Mark where platelets are.
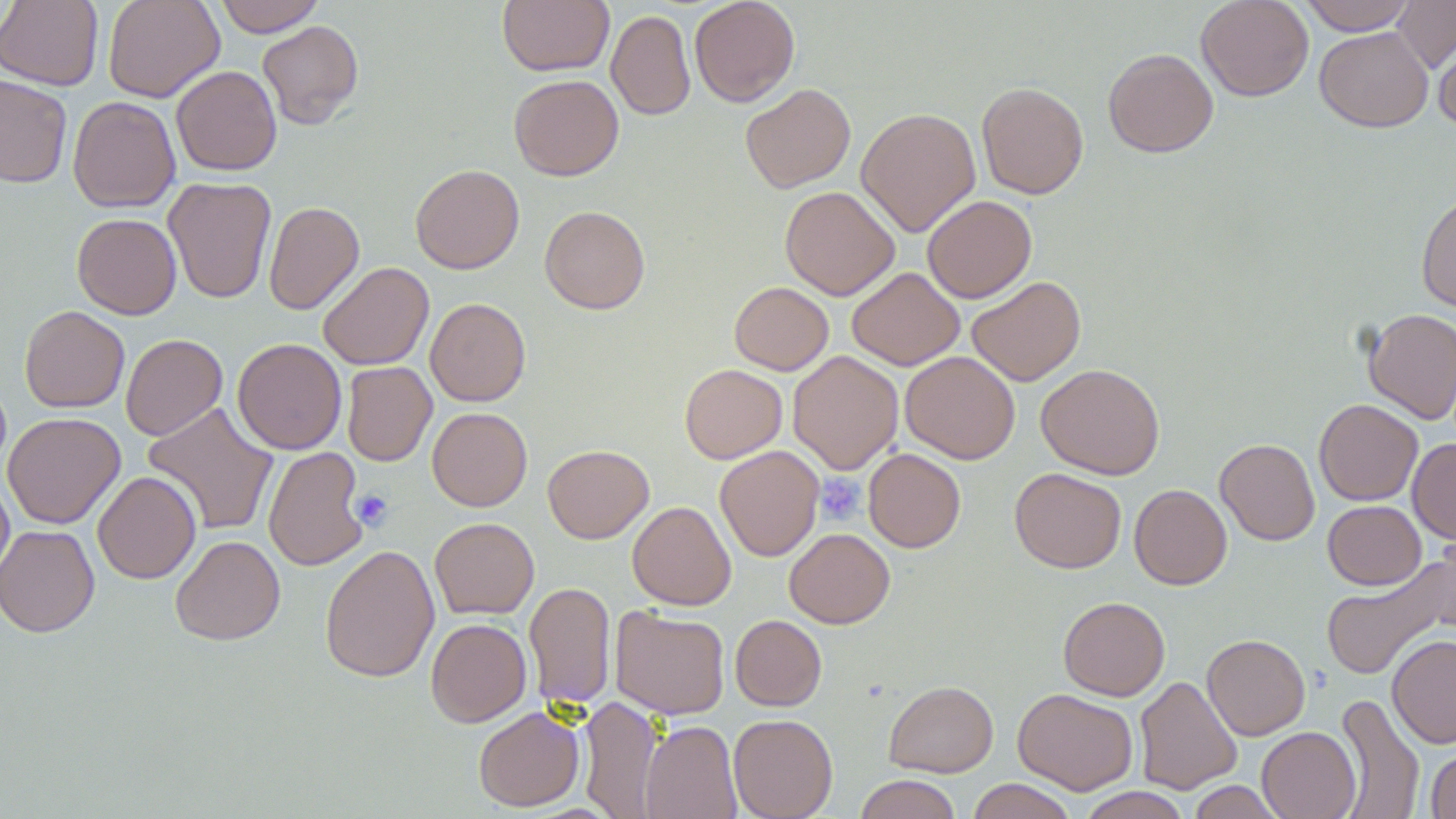

Approximate bounding boxes as (x1,y1)-(x2,y2) corner pairs in pixels.
Platelets: (815,474)-(864,526), (350,488)-(394,531).

Uninfected red blood cell locations: (102,0)-(224,102), (214,0)-(326,36), (497,0)-(614,76), (689,0)-(800,107), (1195,0)-(1314,102), (1299,0)-(1417,35), (1391,0)-(1456,73), (0,1)-(103,90), (606,10)-(695,120), (257,20)-(364,129), (1315,26)-(1433,132), (1432,28)-(1456,133), (1103,48)-(1218,158), (171,66)-(282,175), (509,74)-(624,181), (0,75)-(72,187), (976,82)-(1088,199), (740,83)-(856,193), (68,96)-(181,213), (856,107)-(981,237), (410,164)-(524,274), (163,177)-(277,304), (779,186)-(900,300), (1415,190)-(1456,313), (922,195)-(1037,303), (263,201)-(364,315), (540,206)-(650,314), (71,213)-(182,319), (318,262)-(434,370), (847,267)-(964,370), (966,276)-(1086,386), (729,281)-(833,375), (425,298)-(531,406), (19,305)-(129,413), (1362,308)-(1456,424), (120,333)-(228,440), (232,338)-(346,455), (788,350)-(904,474), (900,351)-(1020,464), (341,361)-(437,467), (1036,363)-(1165,480), (679,364)-(787,464), (1313,399)-(1423,506), (142,402)-(279,536), (427,407)-(532,511), (3,412)-(125,529), (1408,437)-(1456,544), (1215,439)-(1320,545), (542,444)-(654,543), (263,446)-(369,571), (715,446)-(824,561), (863,448)-(966,553), (1009,468)-(1126,573), (92,471)-(201,584), (0,474)-(14,585), (1129,484)-(1232,590), (1323,500)-(1426,590), (627,501)-(736,610), (429,517)-(539,619), (0,525)-(100,637), (784,528)-(895,628), (170,535)-(285,645), (320,544)-(439,683), (1320,561)-(1454,681), (524,581)-(616,711), (1058,596)-(1170,701), (609,606)-(730,719), (730,615)-(827,711), (425,618)-(531,727), (1202,634)-(1310,740), (1387,634)-(1456,748), (1134,675)-(1243,795), (883,680)-(999,777), (1013,688)-(1138,795), (1333,694)-(1425,819), (578,695)-(662,819), (473,706)-(584,811), (728,713)-(838,819), (640,720)-(742,819), (1257,726)-(1361,818), (1425,747)-(1456,818), (854,774)-(962,819), (966,778)-(1077,819), (1187,780)-(1286,819), (1076,787)-(1191,819). Slide-level diagnosis: no evidence of blood parasites. Captured at 1000x magnification. One field of a larger specimen. Thin blood smear. Light microscopy. May-Grünwald-Giemsa-stained preparation. Image is 1456×819 pixels.